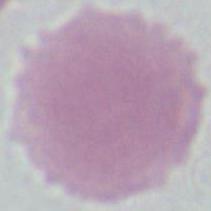
Summary:
  - Magnification: 1000x
  - Modality: micrograph
  - Identification: red blood cell